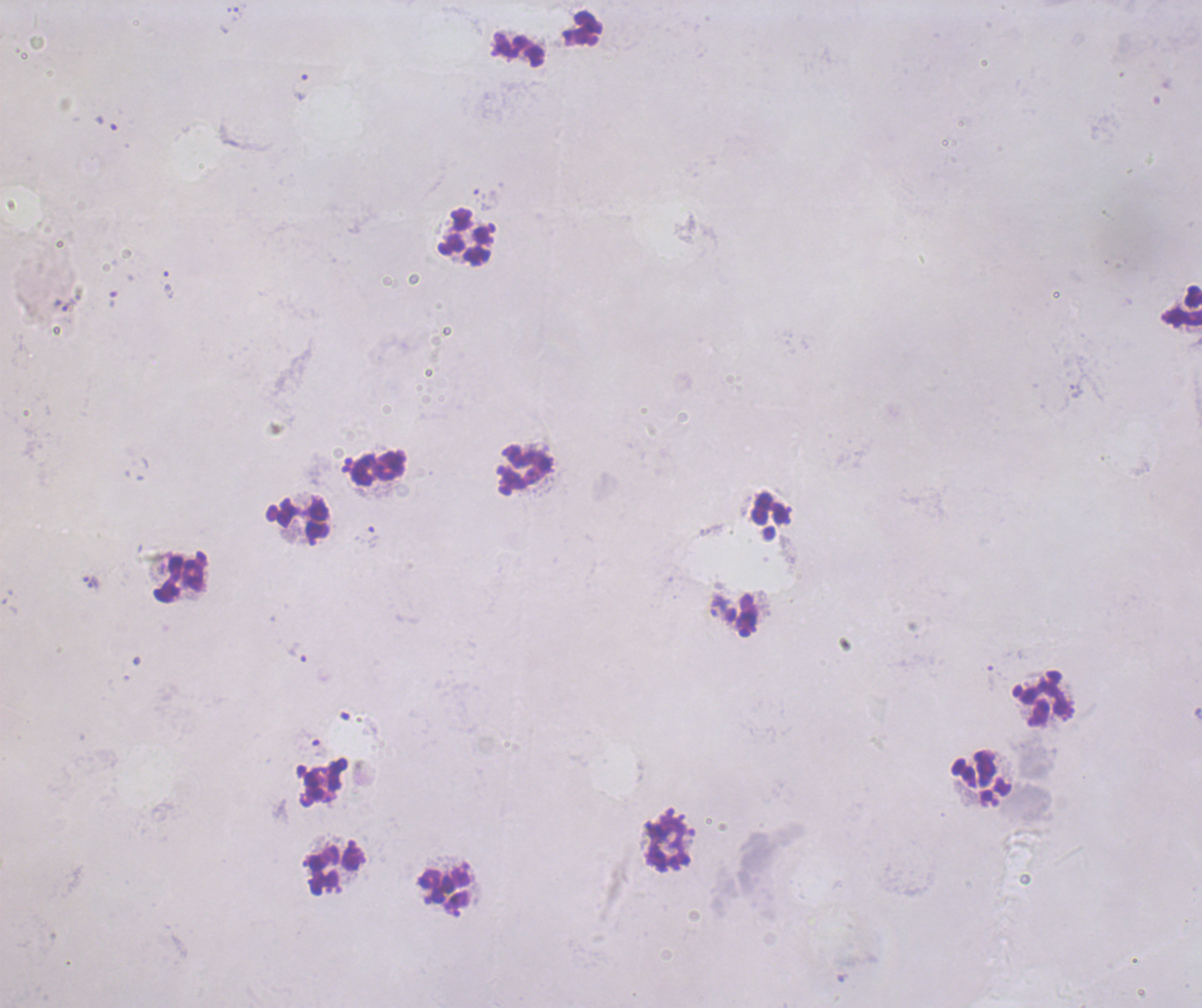
Approximate centers as {x, y} in pixels. Leukocyte locations: {518, 49}, {466, 237}, {1182, 305}, {377, 468}, {525, 469}, {771, 509}, {297, 519}, {180, 578}, {1044, 702}, {981, 779}, {667, 841}, {333, 867}, {447, 890}. Trophozoite locations: {237, 14}, {300, 87}, {167, 281}, {372, 537}, {94, 583}, {297, 652}. Background quality: poor. Image is 1202×1008 pixels. Previously used in an actual diagnosis. Coloration quality: bad. Romanowsky-stained preparation. Thick blood film. Result: malaria parasites identified. Captured at 100x magnification. Single field of view.